Name the parasite shown.
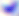
This is Toxoplasma gondii.

Summary:
  - Modality: micrograph
  - Magnification: 400x